Classify this cell by malaria status.
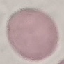

Uninfected.

preparation = thin blood smear
stain = Giemsa
capture = smartphone through the microscope eyepiece
image type = automatically extracted cell patch, resized to 64 × 64 pixels